State which cell type is depicted.
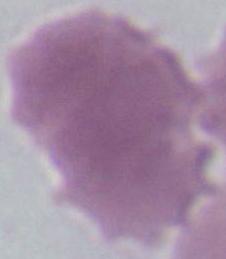

This is an erythrocyte.

magnification = 1000x
modality = photomicrograph